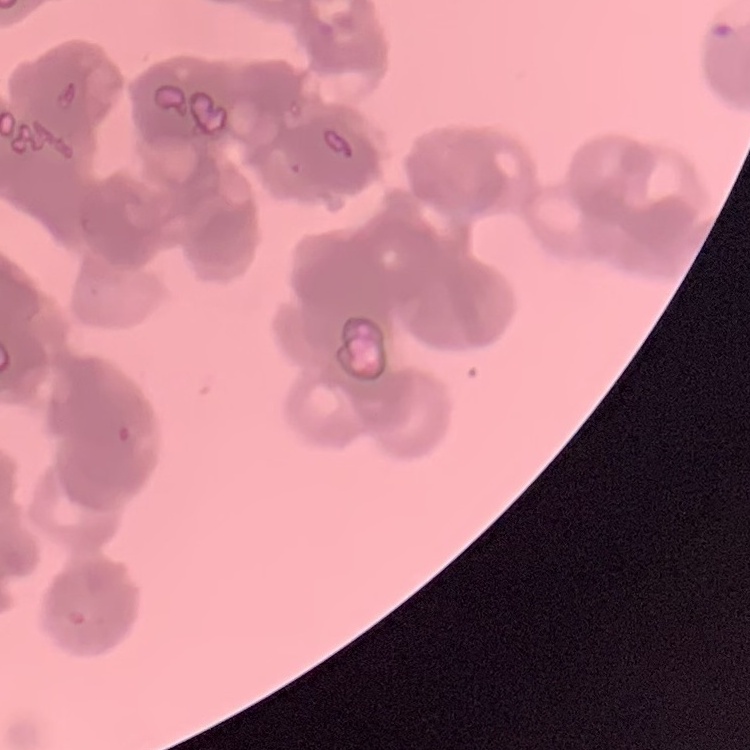
erythrocyte_morphology: rouleaux formation
image_type: one tile cut from a larger photomicrograph
preparation: thin blood film
stain: Field's or Giemsa